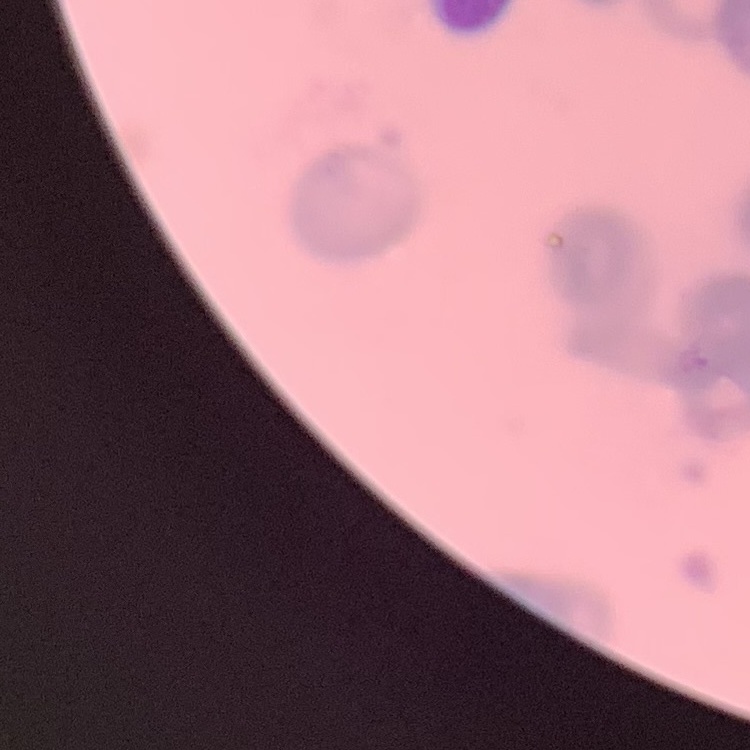
Summary:
  - Red blood cell morphology: rouleaux formation
  - Image type: one tile cut from a larger photomicrograph
  - Stain: Field's or Giemsa
  - Preparation: thin peripheral smear